Comment on the morphology of the erythrocytes.
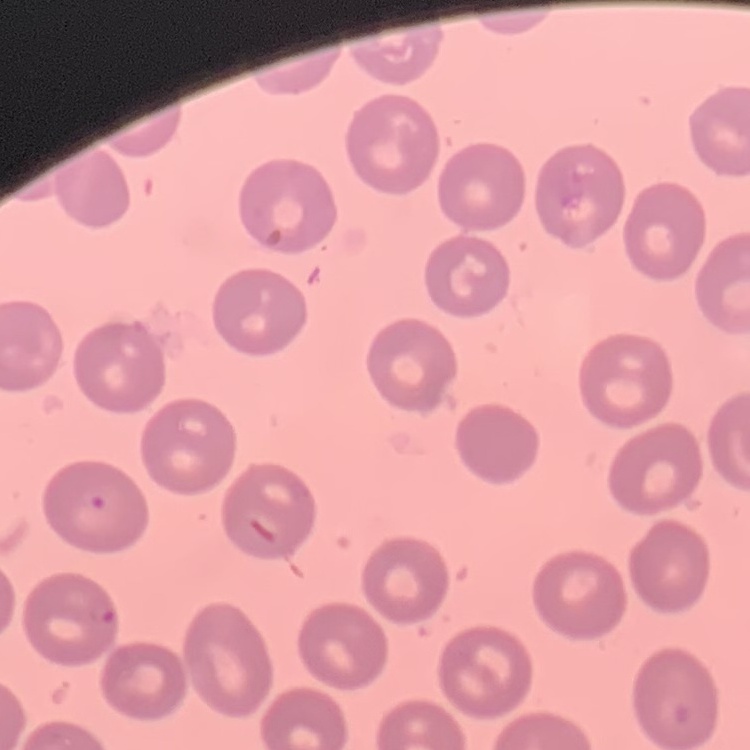

No rouleaux formation.

Square crop of a larger photomicrograph. Thin blood film. Field's or Giemsa stain.